Locate every blood parasite and identify its species.
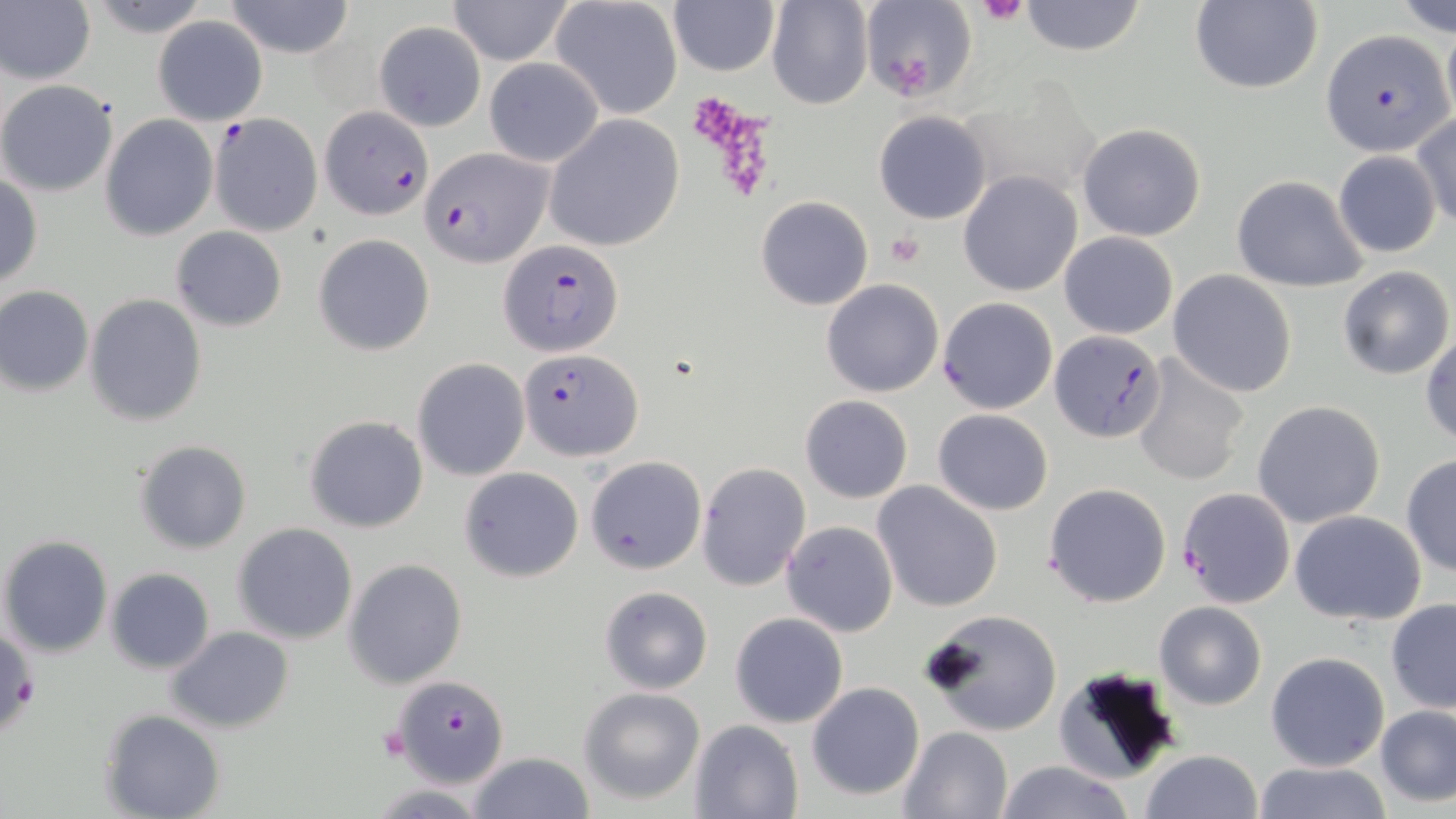

Approximate bounding boxes as (x1,y1)-(x2,y2) corner pairs in pixels.
Plasmodium falciparum-infected red blood cells: (1321,31)-(1452,155), (319,105)-(433,219), (209,113)-(323,236), (422,146)-(551,264), (501,239)-(624,355), (1052,330)-(1166,443), (520,347)-(643,461), (1176,487)-(1296,607).
No Plasmodium ovale, Plasmodium malariae, Plasmodium vivax, Babesia divergens, or Trypanosoma brucei observed.

Summary:
  - Uninfected red blood cell locations: (87,0)-(214,37), (224,0)-(355,58), (446,0)-(576,65), (550,0)-(685,120), (767,0)-(873,109), (859,0)-(975,104), (1019,0)-(1146,56), (1390,0)-(1456,35), (669,1)-(779,77), (1188,1)-(1323,94), (1,2)-(96,84), (151,14)-(269,125), (373,20)-(486,131), (484,57)-(605,166), (0,79)-(119,196), (872,109)-(993,225), (1410,112)-(1456,228), (101,114)-(218,240), (544,114)-(685,252), (1076,124)-(1206,241), (1333,149)-(1442,259), (959,171)-(1083,296), (0,174)-(43,289), (1232,175)-(1368,292), (756,196)-(872,310), (170,227)-(288,331), (1059,232)-(1178,339), (313,234)-(435,356), (1335,265)-(1454,381), (1167,269)-(1298,397), (820,279)-(943,398), (0,285)-(94,396), (85,294)-(206,427), (937,297)-(1058,414), (1421,331)-(1455,448), (1131,353)-(1249,486), (412,358)-(528,481), (799,395)-(912,502), (1251,400)-(1386,528), (932,409)-(1054,514), (305,415)-(428,533), (135,440)-(252,553), (1400,454)-(1456,577), (587,456)-(706,575), (697,462)-(811,591), (458,466)-(583,582), (872,482)-(1003,612), (1043,482)-(1172,608), (1288,509)-(1427,626), (782,521)-(897,637), (232,523)-(359,644), (1,534)-(113,657), (344,559)-(467,688), (106,568)-(214,674), (598,585)-(713,695), (1386,599)-(1456,713), (1155,600)-(1266,710), (922,607)-(1063,737), (730,612)-(849,728), (165,627)-(295,732), (1266,651)-(1391,772), (1056,666)-(1184,782), (390,675)-(509,787), (807,682)-(924,800), (578,686)-(705,804), (1375,706)-(1455,806), (101,710)-(224,819), (689,718)-(803,819), (897,725)-(1015,818), (1140,749)-(1265,819), (468,751)-(595,819), (992,761)-(1138,818), (1252,761)-(1393,818)
  - Platelet locations: (976,0)-(1029,26), (886,231)-(925,268), (377,719)-(411,768)
  - Slide-level diagnosis: Plasmodium falciparum
  - Stain: May-Grünwald-Giemsa
  - Field of view: single
  - Preparation: thin blood smear
  - Image size: 1456×819 pixels
  - Magnification: 1000x
  - Modality: light microscopy